Give the position of every Plasmodium parasite visible.
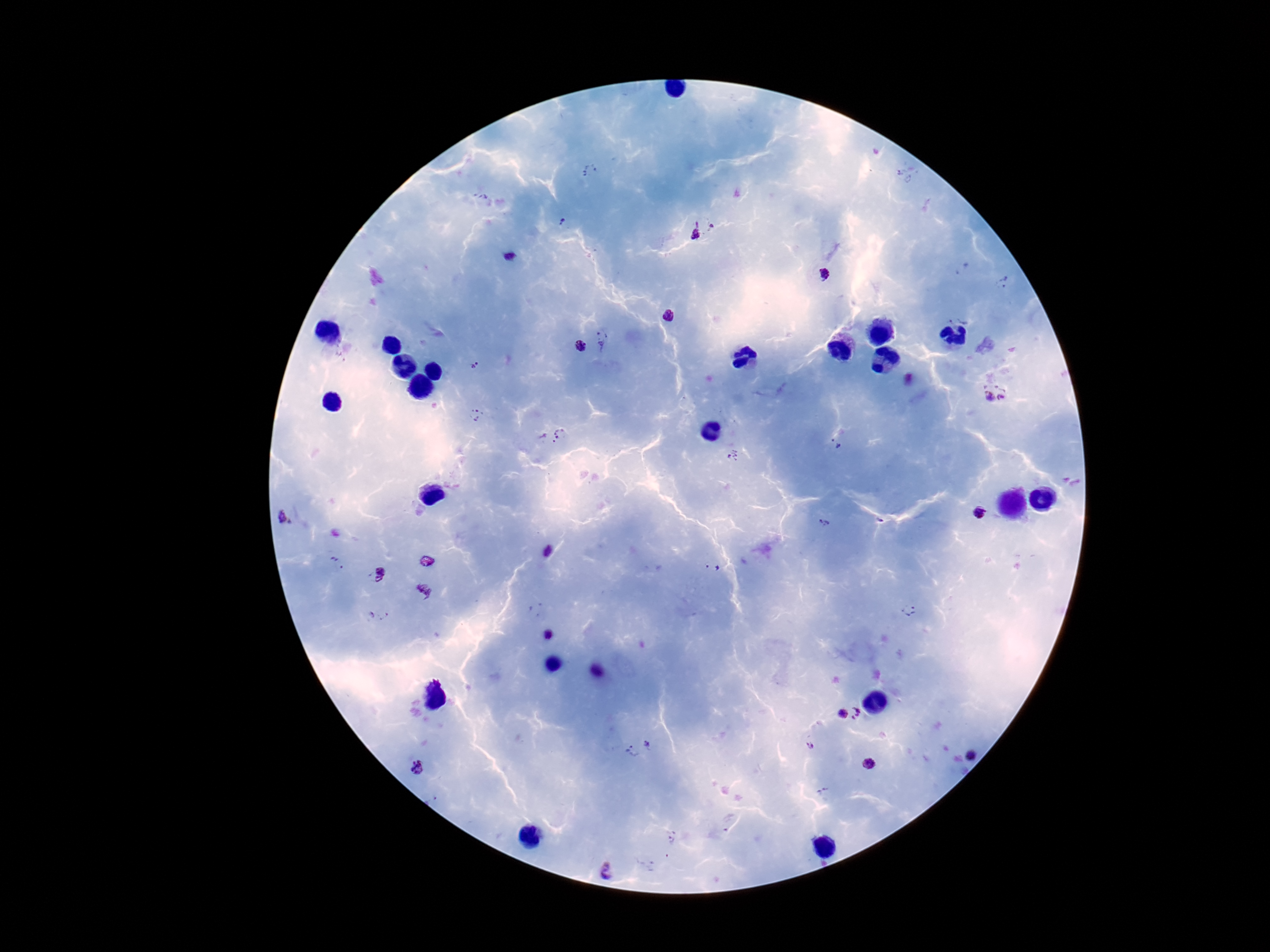

Approximate object centers, in pixels from the top-left corner.
Plasmodium parasites: (x=563, y=223), (x=711, y=226), (x=693, y=231), (x=511, y=257), (x=824, y=276), (x=668, y=315), (x=603, y=339), (x=581, y=346), (x=475, y=366), (x=1002, y=396), (x=987, y=397), (x=476, y=416), (x=561, y=433), (x=546, y=441), (x=836, y=443), (x=734, y=456), (x=979, y=512), (x=281, y=516), (x=291, y=523), (x=824, y=524), (x=551, y=553), (x=714, y=567), (x=380, y=575), (x=423, y=591), (x=908, y=611), (x=385, y=617), (x=548, y=635), (x=857, y=713), (x=842, y=715), (x=647, y=745), (x=810, y=746), (x=634, y=752), (x=971, y=756), (x=867, y=763), (x=417, y=768), (x=822, y=791), (x=607, y=870).

magnification = 100x
field of view = single
patient malaria status = positive
capture = smartphone camera through the microscope eyepiece
preparation = thick peripheral-blood smear
image size = 1270×952 pixels
stain = Giemsa